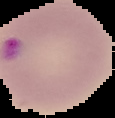

malaria status = parasitized
preparation = thin blood film
image type = cell region segmented out of the field of view; surrounding area masked to black
image size = 115×118 pixels